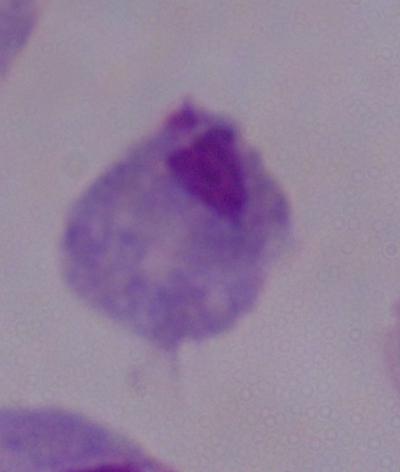
Summary:
  - Modality: micrograph
  - Magnification: 1000x
  - Identification: trichomonad